Outline each uninfected red blood cell.
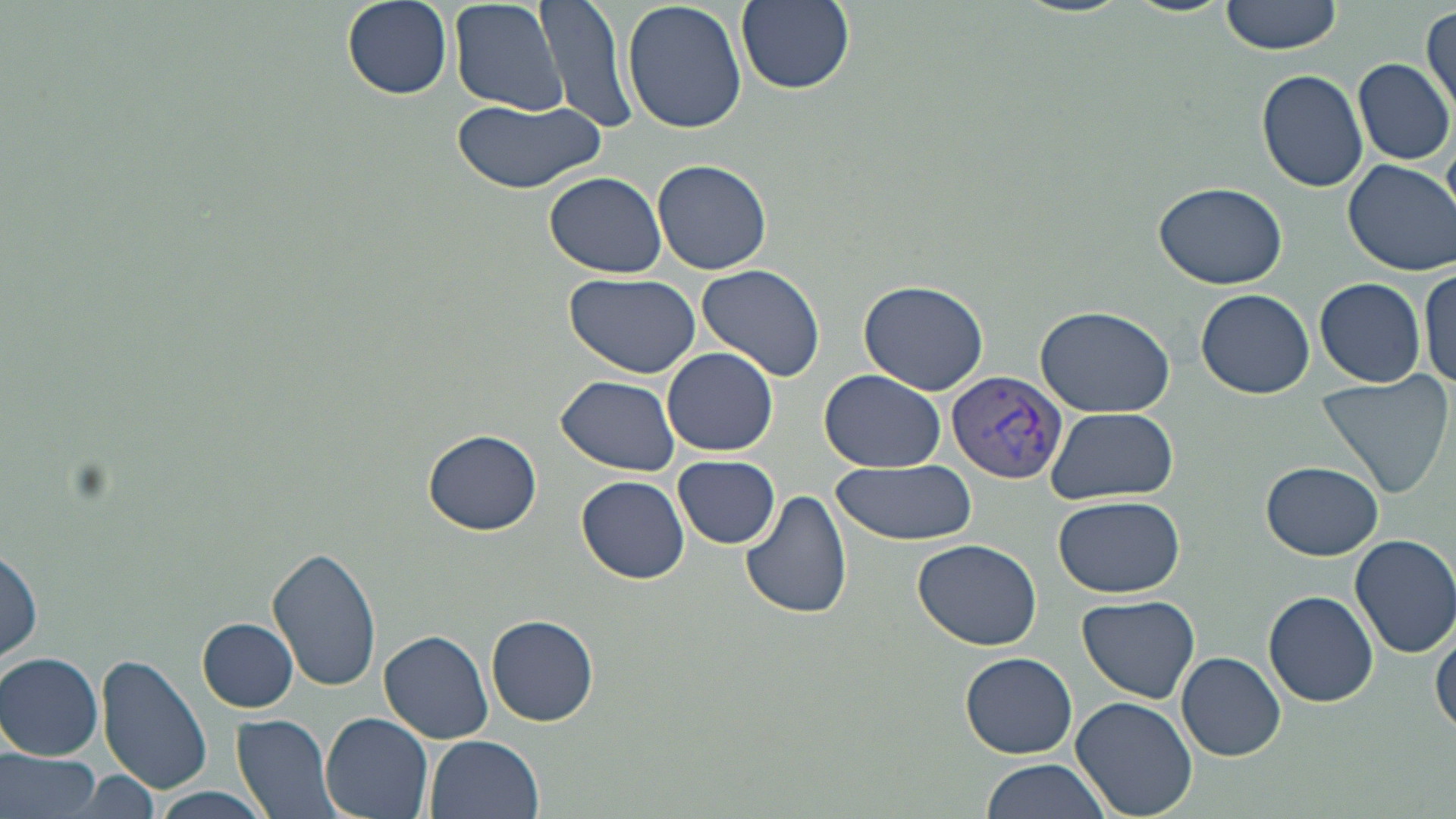
Approximate bounding boxes as (x1,y1)-(x2,y2) corner pairs in pixels.
Uninfected red blood cells: (340,0)-(454,99), (449,0)-(568,118), (534,0)-(641,133), (737,0)-(855,94), (1121,0)-(1232,17), (1220,0)-(1347,57), (623,1)-(747,134), (1420,7)-(1455,113), (1352,58)-(1455,166), (1258,69)-(1369,193), (446,94)-(607,192), (652,158)-(774,276), (1342,159)-(1455,276), (543,171)-(667,277), (1154,180)-(1288,290), (698,263)-(827,384), (1418,265)-(1455,395), (564,272)-(699,379), (1314,277)-(1427,387), (858,279)-(989,393), (1195,288)-(1315,399), (1033,302)-(1175,419), (663,347)-(777,456), (819,369)-(946,473), (1315,370)-(1454,503), (557,374)-(681,476), (1047,406)-(1178,505), (423,430)-(544,534), (674,455)-(780,549), (1262,460)-(1385,560), (828,462)-(976,546), (575,474)-(690,584), (739,487)-(853,622), (1054,494)-(1184,599), (1350,534)-(1456,658), (912,537)-(1043,650), (1,542)-(43,672), (265,542)-(380,690), (1264,591)-(1377,708), (1076,595)-(1203,705), (488,614)-(599,726), (199,619)-(297,712), (1430,619)-(1456,740), (380,631)-(493,744), (1177,651)-(1285,761), (1,652)-(105,759), (960,652)-(1078,760), (97,654)-(213,796), (1069,697)-(1200,819), (320,712)-(432,819), (230,714)-(342,819), (424,734)-(543,818), (1,746)-(103,819), (979,757)-(1115,818), (148,789)-(274,819).

Plasmodium vivax-infected red blood cell locations = approximate bounding boxes as (x1,y1)-(x2,y2) corner pairs in pixels: (946,369)-(1066,484)
slide-level diagnosis = Plasmodium vivax
image size = 1456×819 pixels
magnification = 1000x
modality = optical microscopy
stain = May-Grünwald-Giemsa
preparation = thin blood film
field of view = single